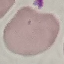

malaria_status: uninfected
stain: Giemsa
preparation: thin smear
capture: smartphone through the microscope eyepiece
image_type: cell patch, automatically extracted from a larger field of view and resized to 64 × 64 pixels